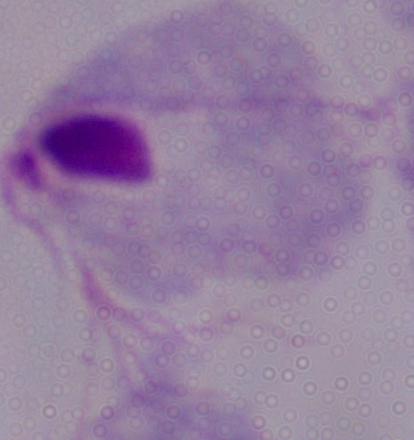
Summary:
  - Identification: trichomonad
  - Magnification: 1000x
  - Modality: micrograph